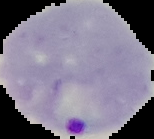

Summary:
  - Malaria status: parasitized
  - Preparation: thin blood smear
  - Image size: 154×139 pixels
  - Image type: segmented cell region with the area outside set to black